Outline each blood parasite and name the species.
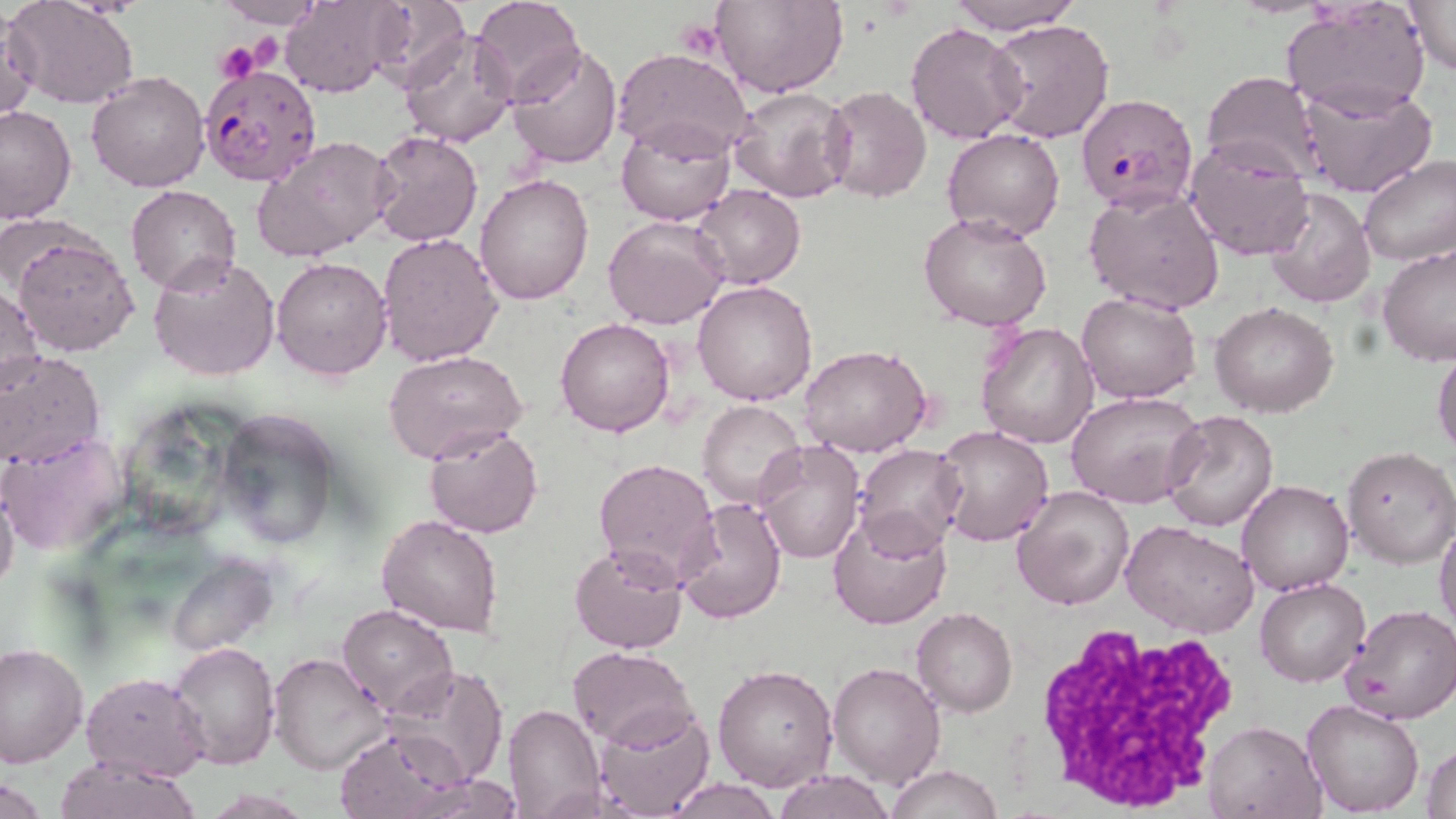

Approximate bounding boxes as named x1/y1/x2/y2 corners in pixels.
Plasmodium falciparum-infected red blood cells: (x1=197, y1=62, x2=324, y2=189), (x1=1078, y1=92, x2=1199, y2=212).
No Plasmodium ovale, Plasmodium malariae, Plasmodium vivax, Babesia divergens, or Trypanosoma brucei observed.

slide-level diagnosis = Plasmodium falciparum
stain = May-Grünwald-Giemsa
preparation = thin blood smear
platelet locations = approximate bounding boxes as named x1/y1/x2/y2 corners in pixels: (x1=677, y1=19, x2=725, y2=58), (x1=212, y1=40, x2=265, y2=83)
modality = light microscopy
uninfected red blood cell locations = approximate bounding boxes as named x1/y1/x2/y2 corners in pixels: (x1=5, y1=0, x2=139, y2=110), (x1=213, y1=0, x2=323, y2=28), (x1=361, y1=0, x2=468, y2=84), (x1=470, y1=0, x2=587, y2=107), (x1=712, y1=0, x2=846, y2=99), (x1=946, y1=0, x2=1081, y2=35), (x1=1403, y1=0, x2=1455, y2=75), (x1=283, y1=1, x2=401, y2=98), (x1=1282, y1=2, x2=1431, y2=118), (x1=0, y1=6, x2=38, y2=126), (x1=986, y1=18, x2=1113, y2=143), (x1=905, y1=22, x2=1026, y2=144), (x1=395, y1=27, x2=520, y2=149), (x1=506, y1=43, x2=622, y2=169), (x1=612, y1=47, x2=754, y2=162), (x1=86, y1=71, x2=210, y2=192), (x1=1201, y1=71, x2=1322, y2=181), (x1=1297, y1=81, x2=1439, y2=200), (x1=823, y1=86, x2=931, y2=203), (x1=729, y1=87, x2=852, y2=203), (x1=0, y1=105, x2=78, y2=224), (x1=616, y1=119, x2=737, y2=227), (x1=942, y1=128, x2=1064, y2=242), (x1=368, y1=129, x2=484, y2=247), (x1=252, y1=135, x2=397, y2=262), (x1=1184, y1=138, x2=1314, y2=261), (x1=1357, y1=154, x2=1456, y2=267), (x1=474, y1=173, x2=595, y2=306), (x1=693, y1=184, x2=806, y2=290), (x1=126, y1=185, x2=240, y2=296), (x1=1262, y1=187, x2=1375, y2=309), (x1=1084, y1=188, x2=1224, y2=314), (x1=920, y1=211, x2=1053, y2=331), (x1=603, y1=216, x2=728, y2=330), (x1=376, y1=231, x2=504, y2=367), (x1=12, y1=232, x2=139, y2=356), (x1=1377, y1=244, x2=1456, y2=367), (x1=148, y1=252, x2=281, y2=382), (x1=271, y1=256, x2=393, y2=381), (x1=694, y1=281, x2=818, y2=405), (x1=0, y1=287, x2=45, y2=399), (x1=1076, y1=290, x2=1202, y2=404), (x1=1211, y1=302, x2=1339, y2=417), (x1=555, y1=317, x2=675, y2=438), (x1=976, y1=320, x2=1099, y2=449), (x1=1432, y1=342, x2=1456, y2=461), (x1=799, y1=345, x2=931, y2=457), (x1=382, y1=350, x2=527, y2=463), (x1=0, y1=351, x2=104, y2=467), (x1=1066, y1=391, x2=1207, y2=510), (x1=698, y1=400, x2=806, y2=513), (x1=217, y1=407, x2=342, y2=548), (x1=1162, y1=410, x2=1280, y2=532), (x1=423, y1=425, x2=544, y2=537), (x1=933, y1=425, x2=1055, y2=548), (x1=0, y1=432, x2=129, y2=555), (x1=754, y1=440, x2=864, y2=566), (x1=851, y1=444, x2=968, y2=552), (x1=401, y1=445, x2=522, y2=613), (x1=1342, y1=447, x2=1455, y2=568), (x1=593, y1=458, x2=721, y2=589), (x1=1237, y1=478, x2=1353, y2=596), (x1=0, y1=481, x2=19, y2=598), (x1=1012, y1=484, x2=1134, y2=611), (x1=676, y1=497, x2=787, y2=625), (x1=827, y1=507, x2=953, y2=630), (x1=377, y1=515, x2=504, y2=638), (x1=1434, y1=516, x2=1456, y2=635), (x1=1122, y1=523, x2=1258, y2=637), (x1=568, y1=542, x2=690, y2=655), (x1=168, y1=557, x2=280, y2=656), (x1=1256, y1=577, x2=1369, y2=688), (x1=336, y1=603, x2=458, y2=716), (x1=1342, y1=605, x2=1456, y2=726), (x1=911, y1=608, x2=1018, y2=717), (x1=171, y1=642, x2=280, y2=771), (x1=0, y1=643, x2=89, y2=769), (x1=567, y1=646, x2=694, y2=749), (x1=271, y1=652, x2=391, y2=774), (x1=828, y1=662, x2=943, y2=786), (x1=712, y1=664, x2=837, y2=793), (x1=385, y1=666, x2=509, y2=785), (x1=82, y1=672, x2=209, y2=782), (x1=1302, y1=699, x2=1424, y2=818), (x1=502, y1=703, x2=603, y2=818), (x1=593, y1=703, x2=715, y2=819), (x1=1203, y1=718, x2=1327, y2=818), (x1=337, y1=729, x2=470, y2=819), (x1=1423, y1=741, x2=1456, y2=819), (x1=53, y1=757, x2=201, y2=819), (x1=886, y1=765, x2=1004, y2=819), (x1=771, y1=769, x2=895, y2=819), (x1=2, y1=777, x2=51, y2=817), (x1=667, y1=777, x2=779, y2=817)
magnification = 1000x
image size = 1456×819 pixels
white blood cell locations = approximate bounding boxes as named x1/y1/x2/y2 corners in pixels: (x1=1026, y1=620, x2=1249, y2=813)
field of view = single